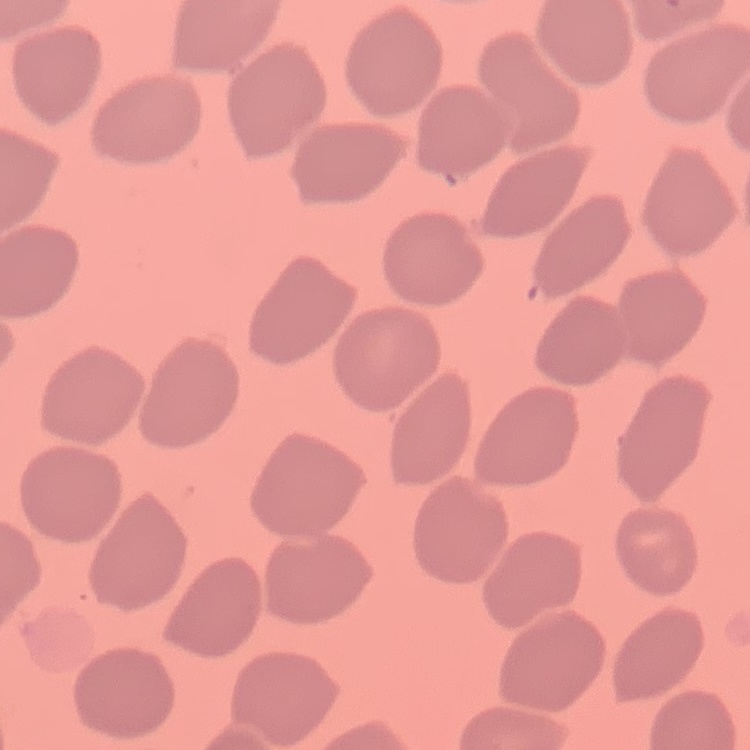

Summary:
  - Erythrocyte morphology: no rouleaux formation
  - Preparation: thin blood film
  - Stain: Field's or Giemsa
  - Image type: square crop of a larger photomicrograph